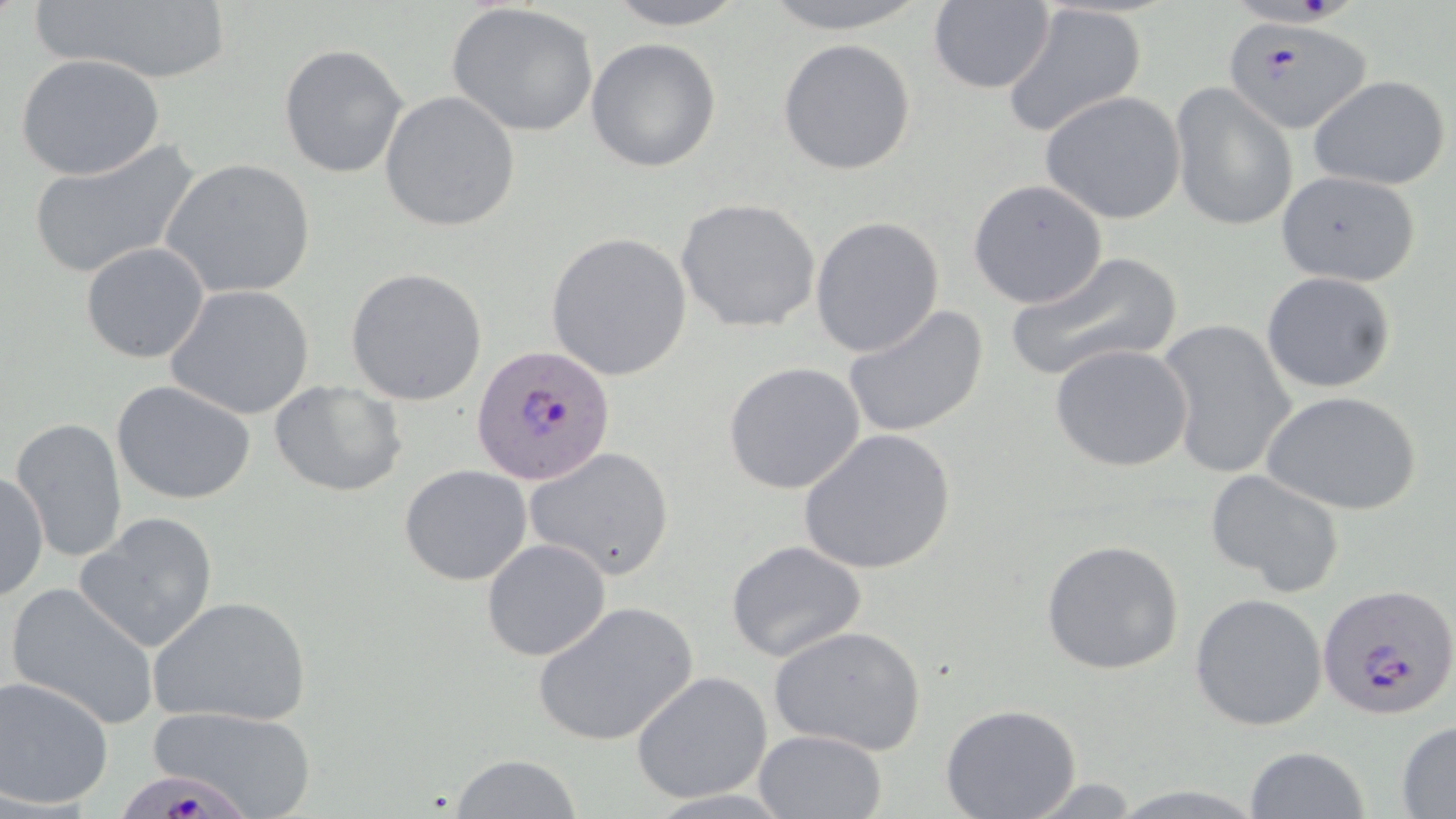
slide-level diagnosis = Plasmodium falciparum
preparation = thin blood film
image size = 1456×819 pixels
field of view = single
Plasmodium falciparum-infected red blood cell locations = approximate bounding boxes as (x1, y1, x2, y2) in pixels: (1235, 0, 1359, 26), (1227, 18, 1377, 134), (471, 343, 618, 486), (1319, 582, 1456, 720), (119, 771, 256, 819)
modality = optical microscopy
uninfected red blood cell locations = approximate bounding boxes as (x1, y1, x2, y2) in pixels: (30, 0, 235, 87), (599, 0, 752, 29), (752, 0, 938, 35), (928, 1, 1056, 95), (448, 2, 600, 139), (1002, 4, 1145, 139), (586, 37, 722, 173), (777, 38, 917, 175), (279, 43, 409, 179), (15, 54, 166, 181), (1308, 73, 1451, 191), (1170, 82, 1297, 231), (378, 91, 520, 232), (1041, 91, 1186, 224), (26, 142, 200, 280), (160, 157, 317, 302), (1276, 169, 1422, 286), (968, 179, 1107, 308), (675, 198, 822, 334), (810, 216, 944, 358), (546, 232, 692, 381), (80, 242, 210, 362), (1005, 250, 1182, 382), (345, 267, 488, 405), (1260, 272, 1396, 394), (165, 285, 316, 421), (841, 304, 989, 440), (1158, 318, 1297, 480), (1049, 343, 1194, 472), (723, 362, 866, 496), (268, 378, 407, 497), (110, 379, 257, 505), (1262, 389, 1424, 517), (11, 417, 127, 563), (797, 429, 958, 574), (523, 447, 675, 579), (399, 464, 532, 586), (1205, 469, 1347, 597), (0, 470, 49, 601), (76, 510, 219, 654), (481, 538, 613, 662), (1040, 539, 1185, 675), (725, 540, 869, 664), (4, 581, 161, 732), (1190, 593, 1328, 731), (148, 595, 312, 728), (532, 602, 698, 747), (768, 624, 927, 755), (631, 671, 774, 806), (1, 675, 115, 808), (939, 702, 1082, 819), (147, 703, 318, 818), (1395, 721, 1456, 815), (754, 729, 886, 818), (1243, 747, 1370, 819), (449, 754, 585, 818), (1020, 776, 1143, 816)
stain = May-Grünwald-Giemsa
magnification = 1000x